Name the cell type shown.
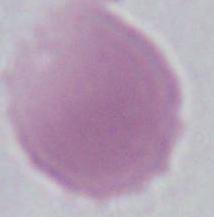

An erythrocyte.

magnification: 1000x
modality: micrograph